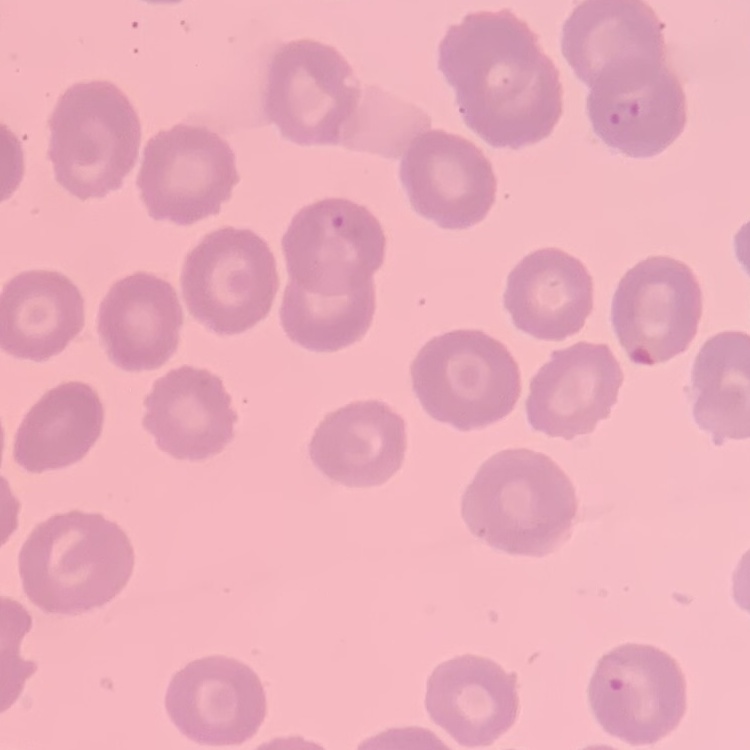

erythrocyte morphology = no rouleaux formation
image type = square crop of a larger photomicrograph
stain = Field's or Giemsa
preparation = thin peripheral smear